Assess this cell for malaria.
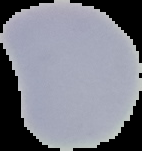

It is uninfected.

Summary:
  - Image size: 142×151 pixels
  - Preparation: thin blood film
  - Image type: segmented cell region with the area outside set to black